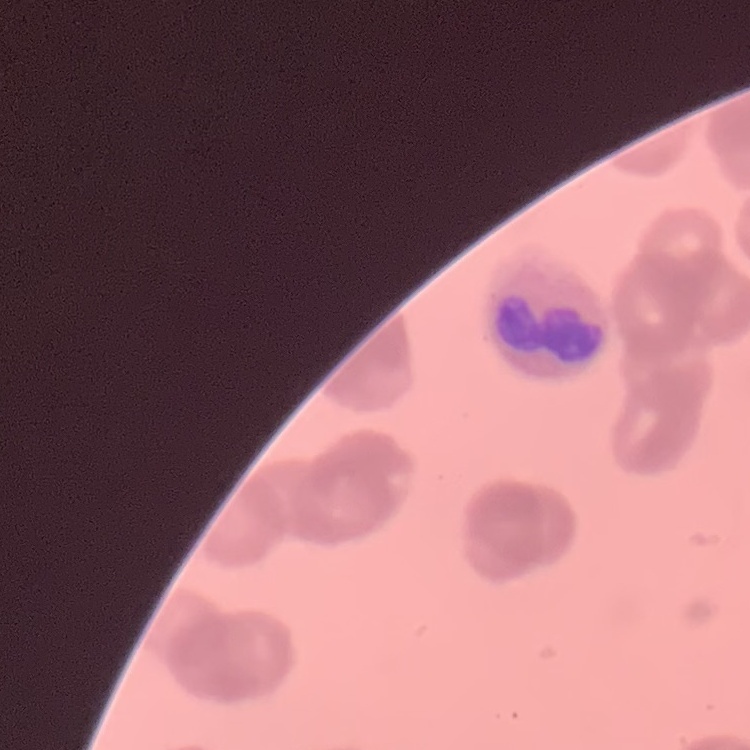

{
  "red_blood_cell_morphology": "rouleaux formation",
  "image_type": "one tile cut from a larger photomicrograph",
  "stain": "Field's or Giemsa",
  "preparation": "thin blood film"
}